Locate every malaria parasite and every leukocyte.
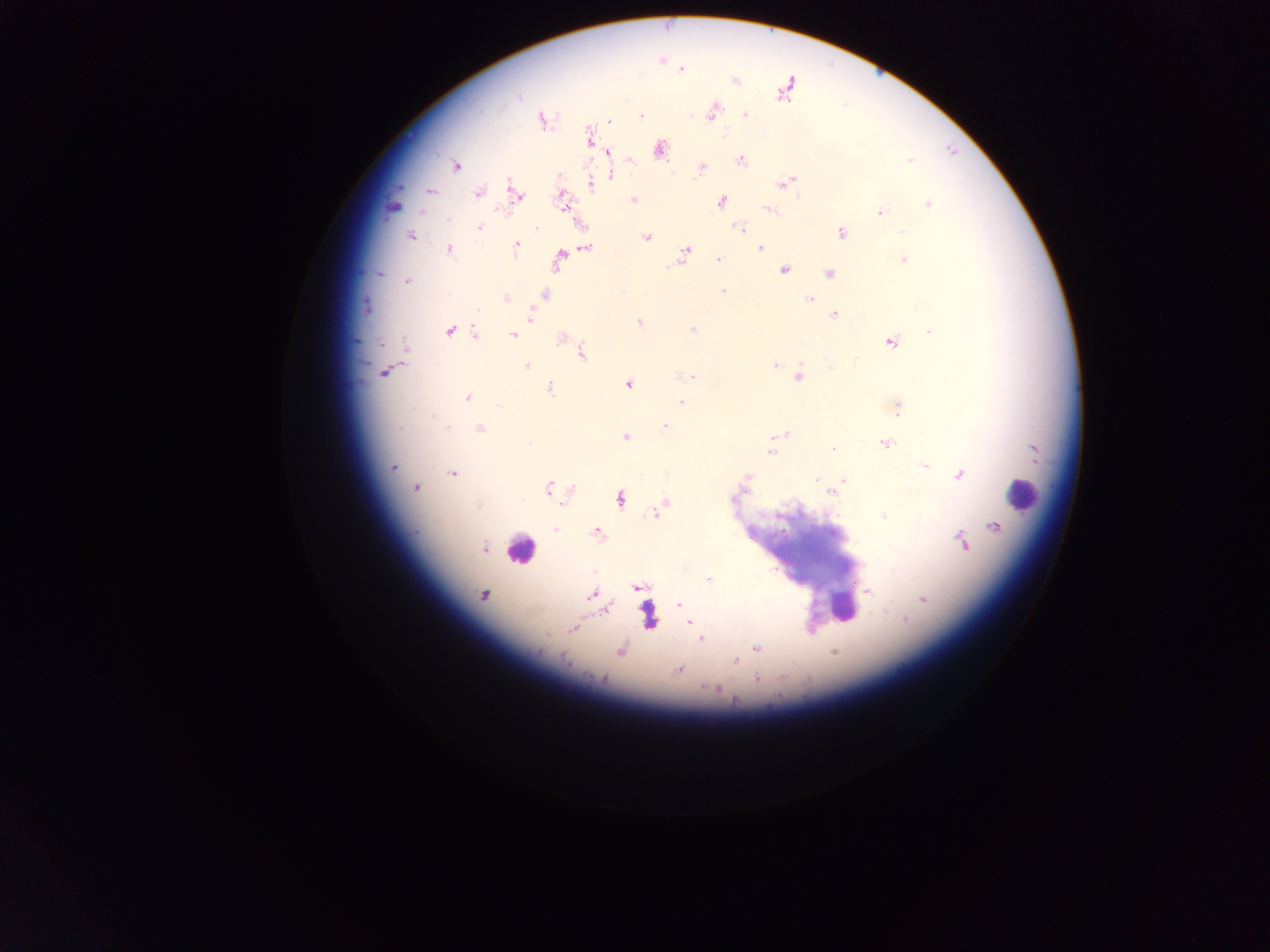
Approximate centers as [x, y] in pixels.
Malaria parasites: [681, 69], [734, 80], [786, 88], [518, 97], [712, 112], [745, 115], [641, 117], [542, 120], [609, 120], [590, 138], [659, 149], [608, 153], [630, 160], [740, 160], [909, 160], [456, 166], [702, 167], [611, 175], [787, 182], [591, 185], [431, 191], [478, 192], [516, 195], [563, 200], [633, 200], [720, 202], [927, 205], [769, 210], [880, 212], [448, 219], [479, 228], [536, 229], [740, 229], [901, 231], [841, 232], [410, 235], [647, 237], [516, 245], [586, 248], [760, 248], [449, 250], [685, 251], [560, 256], [719, 259], [903, 260], [678, 263], [784, 270], [829, 273], [379, 274], [407, 281], [723, 291], [544, 294], [506, 298], [809, 299], [366, 307], [478, 310], [531, 315], [834, 315], [639, 322], [693, 330], [449, 331], [930, 331], [475, 333], [513, 335], [562, 337], [891, 342], [406, 346], [582, 354], [856, 359], [776, 365], [526, 366], [384, 373], [684, 376], [691, 376], [799, 377], [629, 385], [550, 388], [467, 397], [681, 402], [499, 405], [898, 408], [432, 415], [665, 426], [400, 428], [447, 428], [480, 429], [779, 436], [625, 437], [530, 444], [886, 444], [833, 449], [771, 452], [924, 465], [392, 468], [452, 473], [960, 475], [746, 478], [817, 479], [844, 480], [415, 489], [549, 489], [831, 492], [734, 498], [620, 500], [665, 502], [478, 506], [654, 513], [883, 516], [994, 527], [556, 529], [597, 533], [962, 541], [483, 548], [709, 579], [637, 588], [868, 592], [483, 595], [592, 595], [923, 600], [679, 604], [607, 609], [906, 620], [690, 622], [573, 628], [701, 639], [756, 648], [620, 651], [834, 652], [563, 658], [736, 661], [678, 670], [601, 679], [757, 680], [715, 689].
Leukocytes: [395, 203], [1021, 493], [520, 550], [842, 605], [647, 616].

image size = 1270×952 pixels
capture = mobile-phone photograph through a microscope
field of view = single
preparation = thick blood smear
country = Ghana